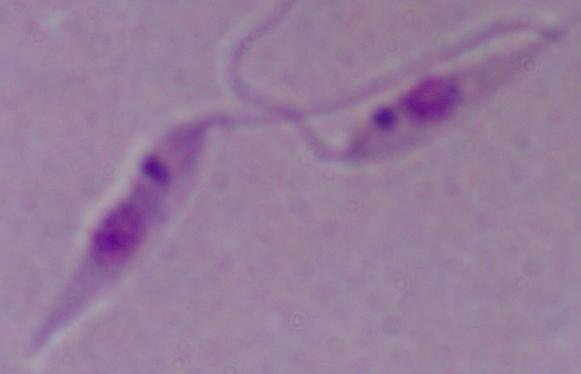
modality = micrograph
identification = Leishmania
magnification = 1000x